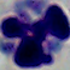
modality: micrograph
identification: leukocyte
magnification: 1000x